Report the malaria status of this cell.
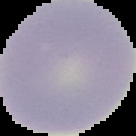
It is uninfected.

Segmented cell region on a black background. From a thin blood film. Image is 136×136 pixels.